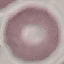
malaria status = uninfected
capture = smartphone through the microscope eyepiece
preparation = thin smear
image type = cell patch, automatically extracted from a larger field of view and resized to 64 × 64 pixels
stain = Giemsa